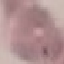
result = no malaria parasites seen
image type = cell patch, automatically extracted from a larger field of view and resized to 64 × 64 pixels
stain = Giemsa
preparation = thin blood film
capture = smartphone through the microscope eyepiece